Classify this cell by malaria status.
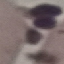

It is uninfected.

stain = Giemsa
capture = smartphone camera at the microscope eyepiece
image type = automatically extracted cell patch, resized to 64 × 64 pixels
preparation = thin blood smear